Report the malaria status of this cell.
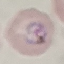

It is parasitized.

Summary:
  - Image type: cell patch, automatically extracted from a larger field of view and resized to 64 × 64 pixels
  - Preparation: thin smear
  - Stain: Giemsa
  - Capture: smartphone through the microscope eyepiece